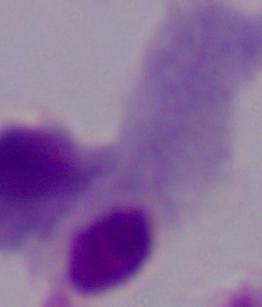
magnification = 1000x
modality = micrograph
identification = trichomonad